Assess the morphology of the red blood cells.
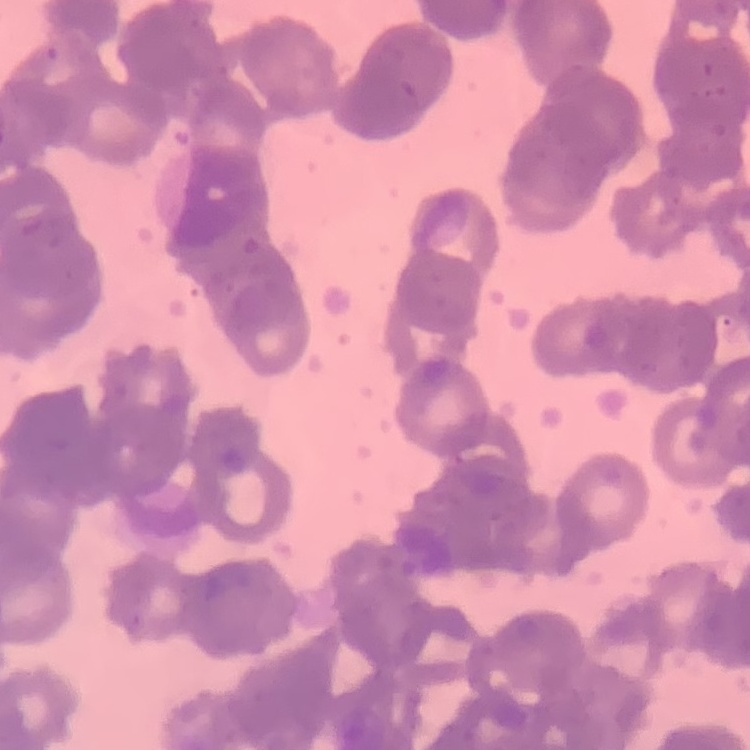
Rouleaux formation.

Square crop of a larger photomicrograph. Thin peripheral smear. Field's or Giemsa stain.